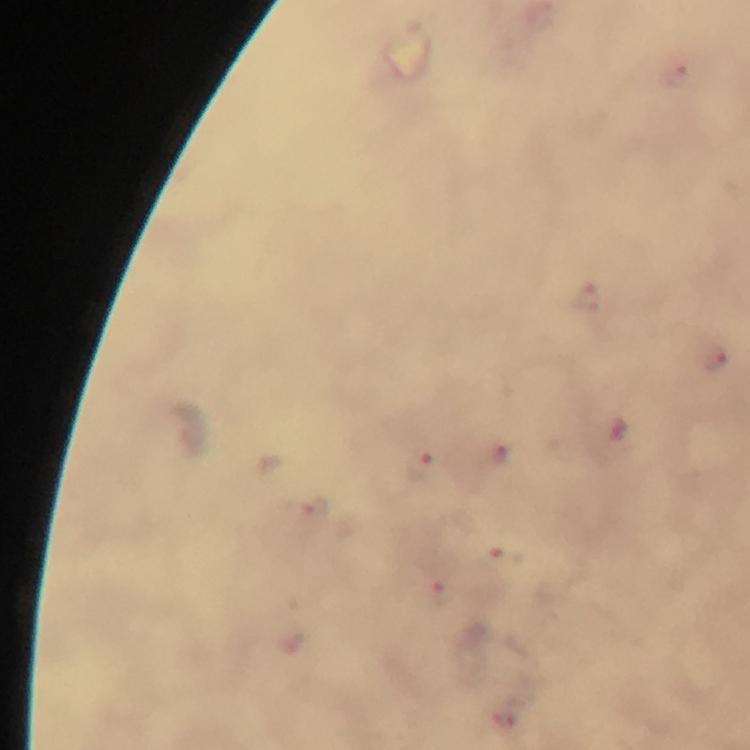

Approximate centers as (x, y) in pixels.
Summary:
  - Malaria parasite locations: (676, 75), (591, 299), (714, 359), (499, 454), (421, 468), (314, 508), (509, 556), (439, 597)
  - Capture: smartphone mounted on the microscope
  - Preparation: thick blood smear
  - Immersion oil: applied
  - Stain: Giemsa
  - Context: from a malaria diagnostic workup
  - Cropped from: a single field of view
  - Magnification: 100x
  - Image size: 750×750 pixels